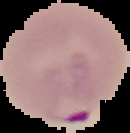

Summary:
  - Preparation: thin blood film
  - Image size: 130×133 pixels
  - Image type: segmented cell region with the area outside set to black
  - Result: malaria parasites identified